Report the malaria status.
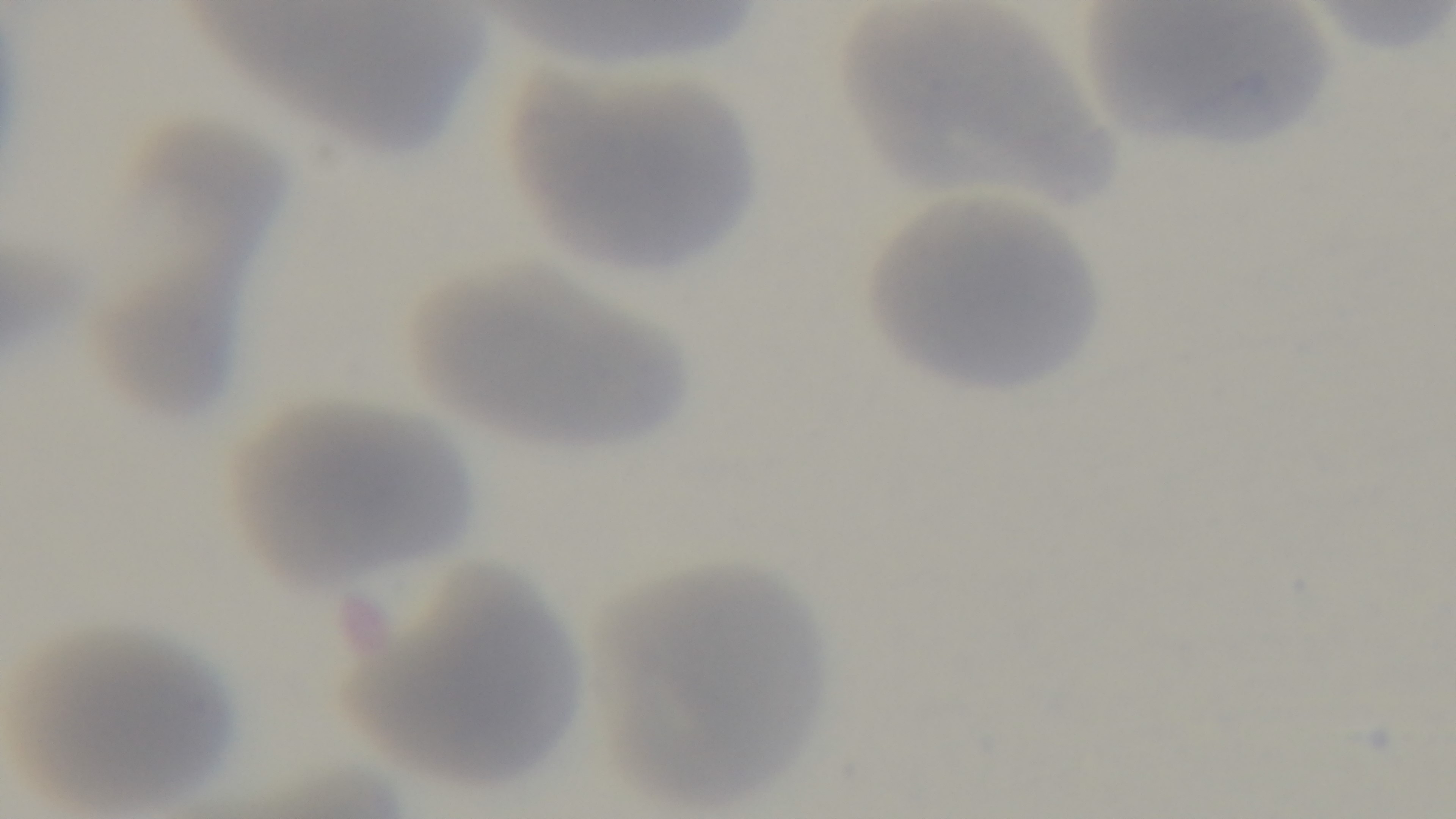
It is uninfected.

Single field of view. Mounted 4K digital camera. Photomicrograph. Preparation: thin smear. Giemsa-stained. Oil-immersion objective, 100x.